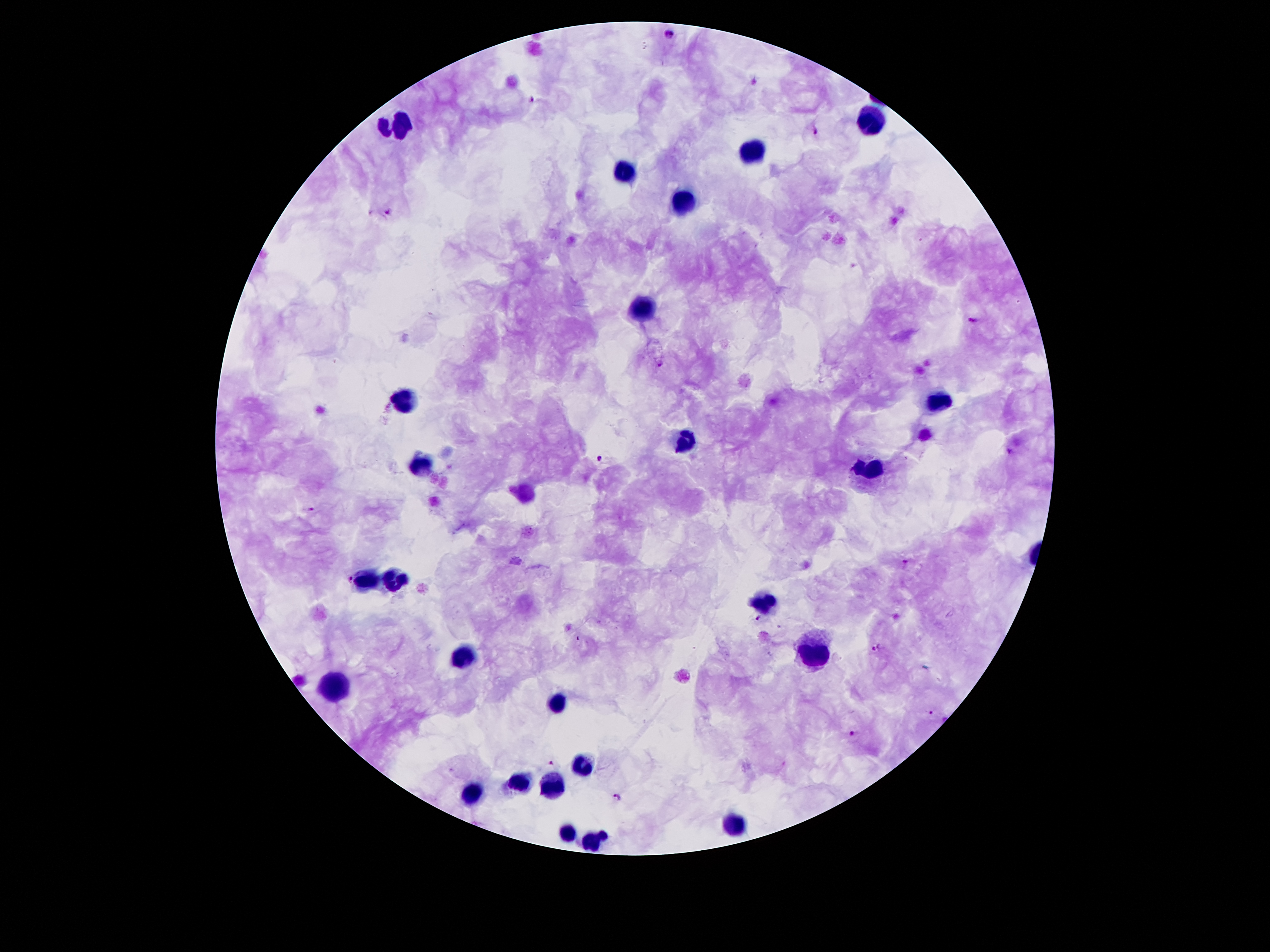

patient_malaria_status: positive for Plasmodium falciparum
image_size: 1270×952 pixels
leukocyte_locations: 'approximate object centers, in pixels from the top-left corner: (x=872, y=118), (x=397, y=126), (x=750, y=152), (x=622, y=170), (x=682, y=204), (x=644, y=307), (x=404, y=400), (x=941, y=402), (x=686, y=441), (x=424, y=464), (x=870, y=467), (x=396, y=580), (x=366, y=582), (x=762, y=600), (x=814, y=652), (x=465, y=657), (x=334, y=685), (x=558, y=703), (x=584, y=768), (x=520, y=781), (x=556, y=786), (x=474, y=794), (x=737, y=822), (x=566, y=830), (x=592, y=841)'
preparation: thick blood film
field_of_view: one from this slide
stain: Giemsa
capture: smartphone camera through the microscope eyepiece
plasmodium_parasite_locations: 'approximate object centers, in pixels from the top-left corner: (x=671, y=32), (x=534, y=99), (x=815, y=132), (x=388, y=212), (x=972, y=319), (x=660, y=364), (x=1009, y=451), (x=601, y=460), (x=310, y=509), (x=351, y=580), (x=757, y=617), (x=875, y=649), (x=931, y=713), (x=853, y=733), (x=551, y=763), (x=618, y=797)'
magnification: 100x